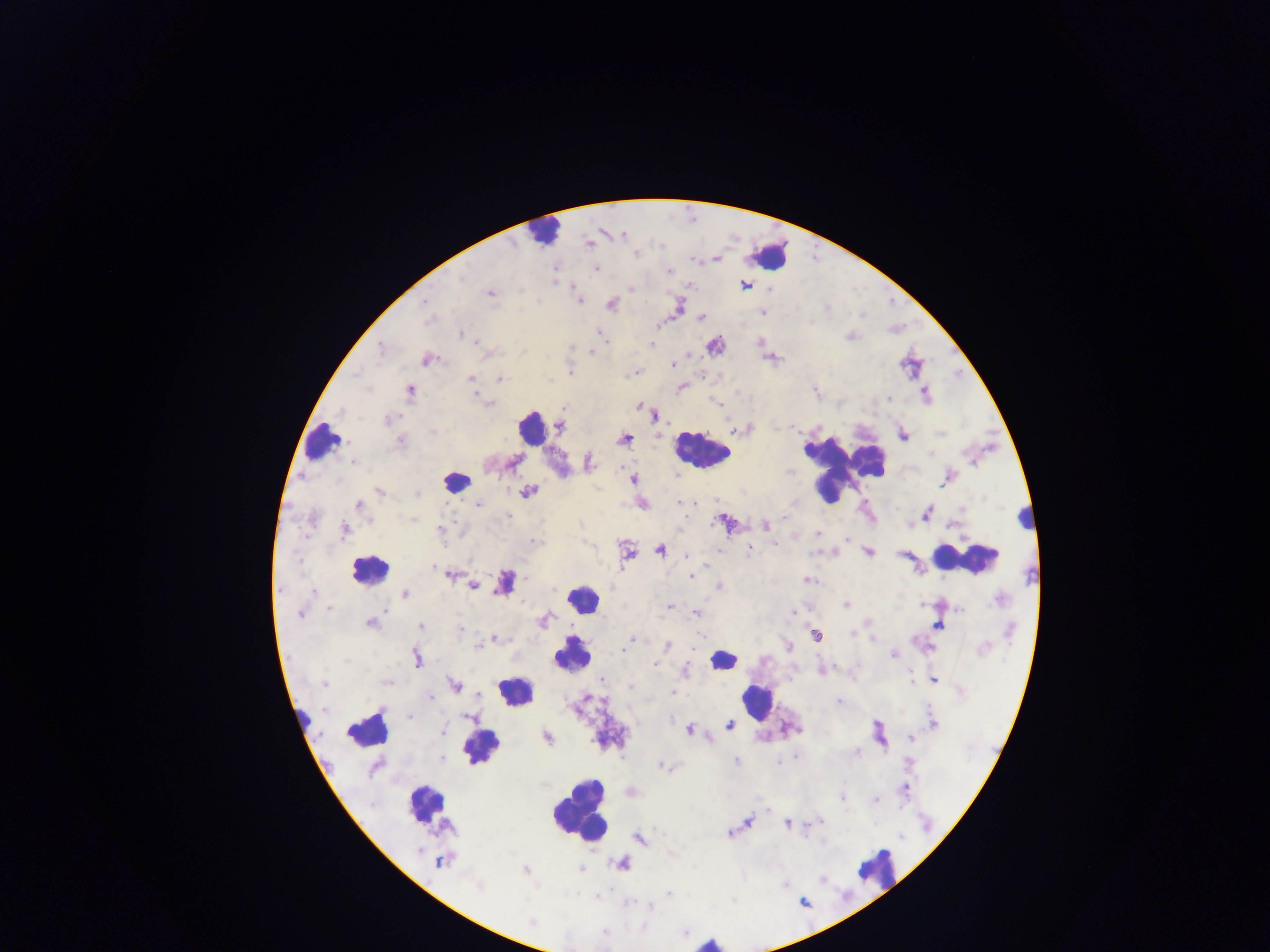

Approximate centers as {x, y} in pixels. Object labeled both malaria parasite and leukocyte by the source: {505, 582}. Malaria parasite locations: {621, 234}, {588, 243}, {636, 253}, {716, 258}, {596, 268}, {669, 271}, {553, 279}, {744, 284}, {768, 287}, {631, 289}, {489, 293}, {579, 299}, {425, 303}, {611, 304}, {678, 305}, {763, 311}, {701, 317}, {656, 324}, {598, 332}, {462, 334}, {759, 342}, {651, 344}, {714, 344}, {380, 348}, {591, 352}, {486, 353}, {771, 357}, {426, 358}, {672, 365}, {570, 372}, {635, 372}, {470, 378}, {499, 379}, {681, 387}, {409, 390}, {816, 392}, {925, 393}, {475, 394}, {888, 398}, {489, 403}, {639, 406}, {654, 413}, {389, 420}, {559, 425}, {741, 429}, {902, 433}, {623, 439}, {399, 440}, {513, 461}, {353, 462}, {588, 462}, {789, 471}, {632, 479}, {946, 479}, {380, 491}, {527, 491}, {416, 494}, {678, 501}, {694, 501}, {479, 503}, {641, 503}, {358, 505}, {927, 513}, {413, 519}, {724, 522}, {909, 524}, {766, 525}, {343, 528}, {440, 529}, {817, 534}, {847, 539}, {775, 543}, {659, 549}, {718, 550}, {749, 550}, {868, 551}, {834, 552}, {626, 553}, {903, 553}, {686, 555}, {432, 566}, {451, 574}, {692, 575}, {808, 580}, {472, 585}, {718, 586}, {313, 592}, {404, 594}, {846, 604}, {669, 606}, {328, 608}, {299, 613}, {697, 613}, {793, 613}, {543, 620}, {869, 622}, {370, 623}, {937, 623}, {420, 626}, {460, 629}, {851, 632}, {816, 635}, {871, 637}, {496, 638}, {631, 639}, {788, 645}, {667, 646}, {478, 647}, {893, 654}, {417, 658}, {654, 663}, {822, 670}, {685, 671}, {908, 671}, {933, 679}, {602, 680}, {386, 682}, {323, 683}, {454, 685}, {629, 686}, {671, 693}, {838, 703}, {409, 717}, {469, 717}, {933, 724}, {729, 725}, {688, 729}, {440, 731}, {879, 732}, {546, 737}, {911, 738}, {857, 751}, {796, 756}, {734, 760}, {663, 765}, {905, 789}, {630, 792}, {842, 796}, {876, 799}, {820, 821}, {748, 822}, {787, 824}, {729, 833}, {638, 838}, {442, 860}, {621, 864}, {581, 868}, {526, 869}, {821, 878}, {478, 886}, {670, 893}. Leukocyte locations: {543, 231}, {769, 256}, {532, 427}, {320, 440}, {700, 450}, {840, 466}, {456, 481}, {1024, 518}, {967, 559}, {369, 568}, {582, 599}, {572, 653}, {723, 658}, {516, 690}, {756, 701}, {368, 728}, {479, 747}, {424, 802}, {579, 811}, {876, 867}, {709, 942}. Thick blood smear. Image is 1270×952 pixels. Mobile-phone photograph taken through the microscope. Collected in Ghana. Single field of view.